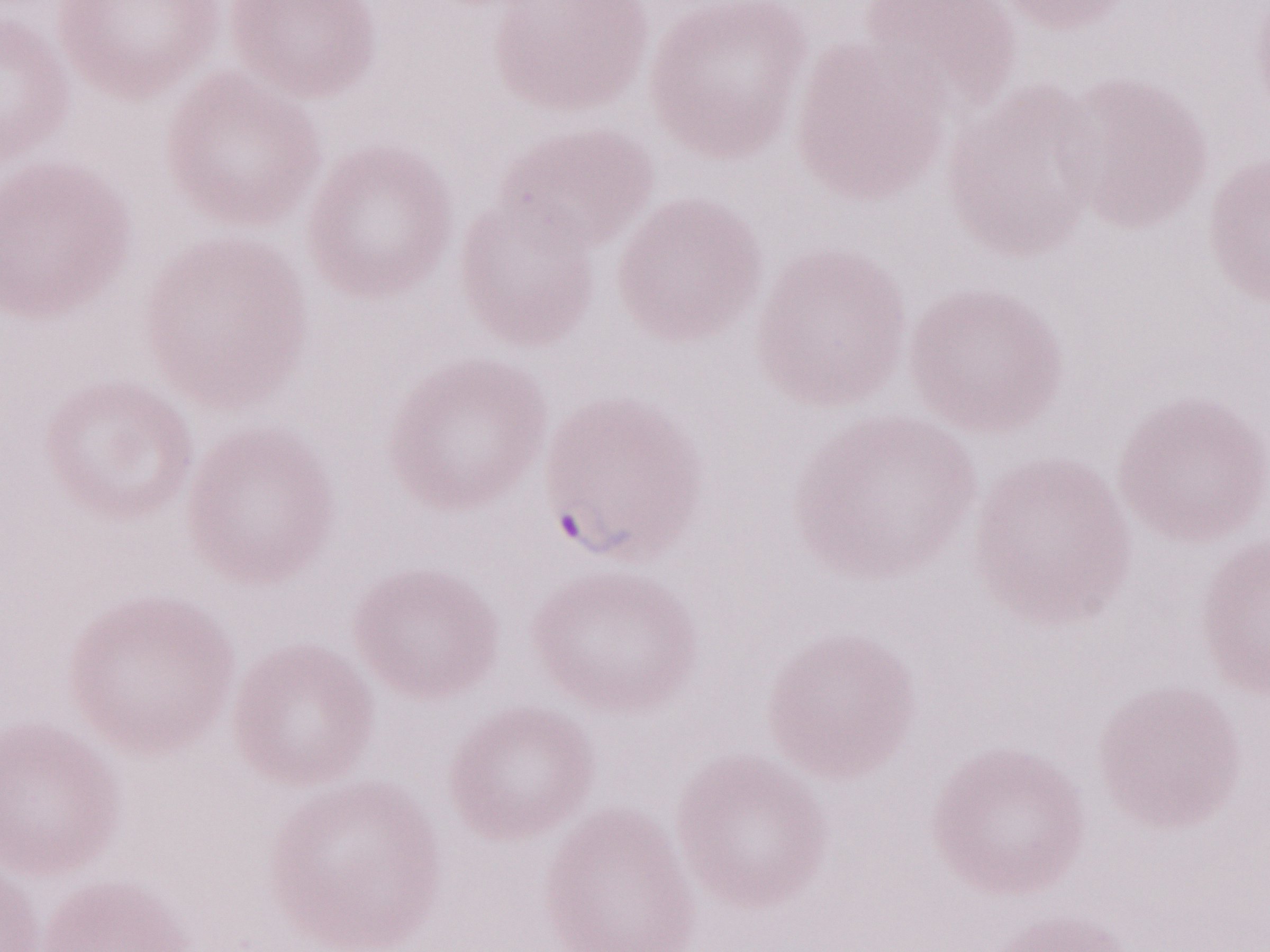
Thin blood smear. Image is 1270×952 pixels. One field of this slide. Olympus BX43 microscope and DP73 digital camera. 1,000x magnification. Patient diagnosis: malaria infection. May-Grünwald-Giemsa-stained preparation.